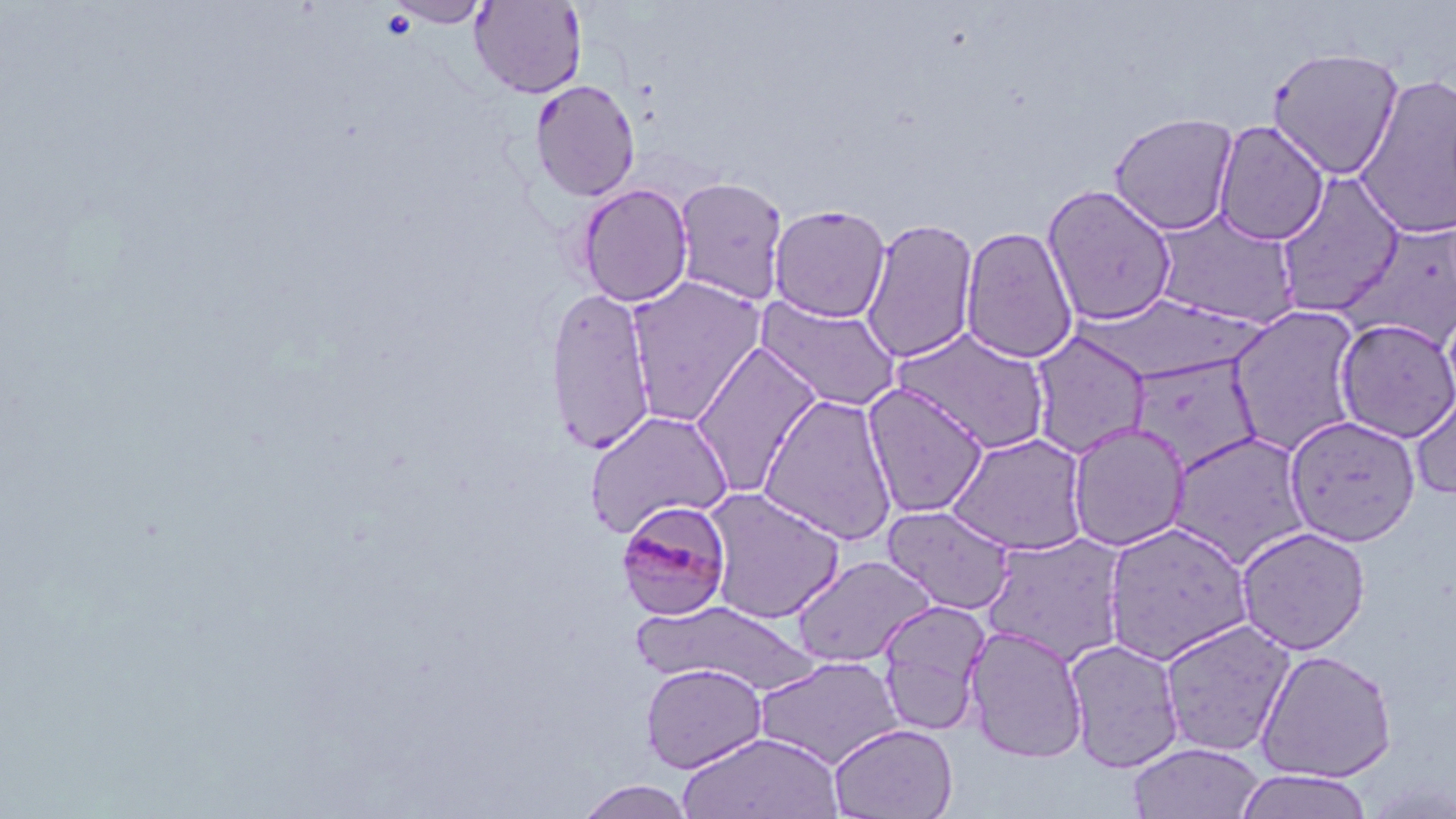

Summary:
  - Coordinate format: approximate bounding boxes as named x1/y1/x2/y2 corners in pixels
  - Plasmodium malariae-infected red blood cell locations: (x1=617, y1=499, x2=733, y2=622)
  - Uninfected red blood cell locations: (x1=387, y1=0, x2=491, y2=27), (x1=469, y1=0, x2=587, y2=99), (x1=1266, y1=47, x2=1405, y2=180), (x1=1353, y1=73, x2=1455, y2=242), (x1=529, y1=79, x2=641, y2=202), (x1=1108, y1=112, x2=1240, y2=236), (x1=1212, y1=121, x2=1329, y2=246), (x1=1274, y1=173, x2=1405, y2=316), (x1=672, y1=177, x2=790, y2=305), (x1=576, y1=183, x2=694, y2=307), (x1=1041, y1=184, x2=1179, y2=327), (x1=768, y1=203, x2=891, y2=323), (x1=1148, y1=207, x2=1300, y2=328), (x1=859, y1=217, x2=979, y2=364), (x1=1335, y1=221, x2=1456, y2=354), (x1=960, y1=225, x2=1079, y2=365), (x1=624, y1=274, x2=767, y2=424), (x1=544, y1=285, x2=657, y2=454), (x1=756, y1=296, x2=902, y2=413), (x1=1227, y1=304, x2=1364, y2=456), (x1=1334, y1=317, x2=1456, y2=443), (x1=892, y1=327, x2=1055, y2=455), (x1=1029, y1=331, x2=1151, y2=458), (x1=690, y1=339, x2=824, y2=499), (x1=1126, y1=353, x2=1262, y2=475), (x1=862, y1=382, x2=989, y2=519), (x1=1409, y1=383, x2=1456, y2=501), (x1=759, y1=392, x2=899, y2=545), (x1=582, y1=409, x2=733, y2=538), (x1=1284, y1=414, x2=1421, y2=546), (x1=1066, y1=421, x2=1190, y2=552), (x1=945, y1=431, x2=1089, y2=556), (x1=1168, y1=431, x2=1313, y2=569), (x1=701, y1=486, x2=845, y2=624), (x1=881, y1=503, x2=1017, y2=615), (x1=1102, y1=520, x2=1255, y2=665), (x1=1235, y1=525, x2=1371, y2=655), (x1=980, y1=532, x2=1130, y2=666), (x1=791, y1=554, x2=937, y2=667), (x1=629, y1=600, x2=820, y2=695), (x1=876, y1=600, x2=991, y2=734), (x1=1158, y1=617, x2=1297, y2=758), (x1=964, y1=624, x2=1089, y2=763), (x1=1064, y1=637, x2=1185, y2=773), (x1=1255, y1=649, x2=1398, y2=783), (x1=752, y1=655, x2=905, y2=770), (x1=640, y1=662, x2=769, y2=774), (x1=828, y1=723, x2=958, y2=819), (x1=677, y1=731, x2=844, y2=818), (x1=1127, y1=741, x2=1265, y2=819), (x1=1234, y1=770, x2=1376, y2=818), (x1=572, y1=779, x2=699, y2=819)
  - Slide-level diagnosis: Plasmodium malariae
  - Preparation: thin blood film
  - Magnification: 1000x
  - Modality: light microscopy
  - Stain: May-Grünwald-Giemsa
  - Image size: 1456×819 pixels
  - Field of view: single